Give a bounding box for every leukocyte visible.
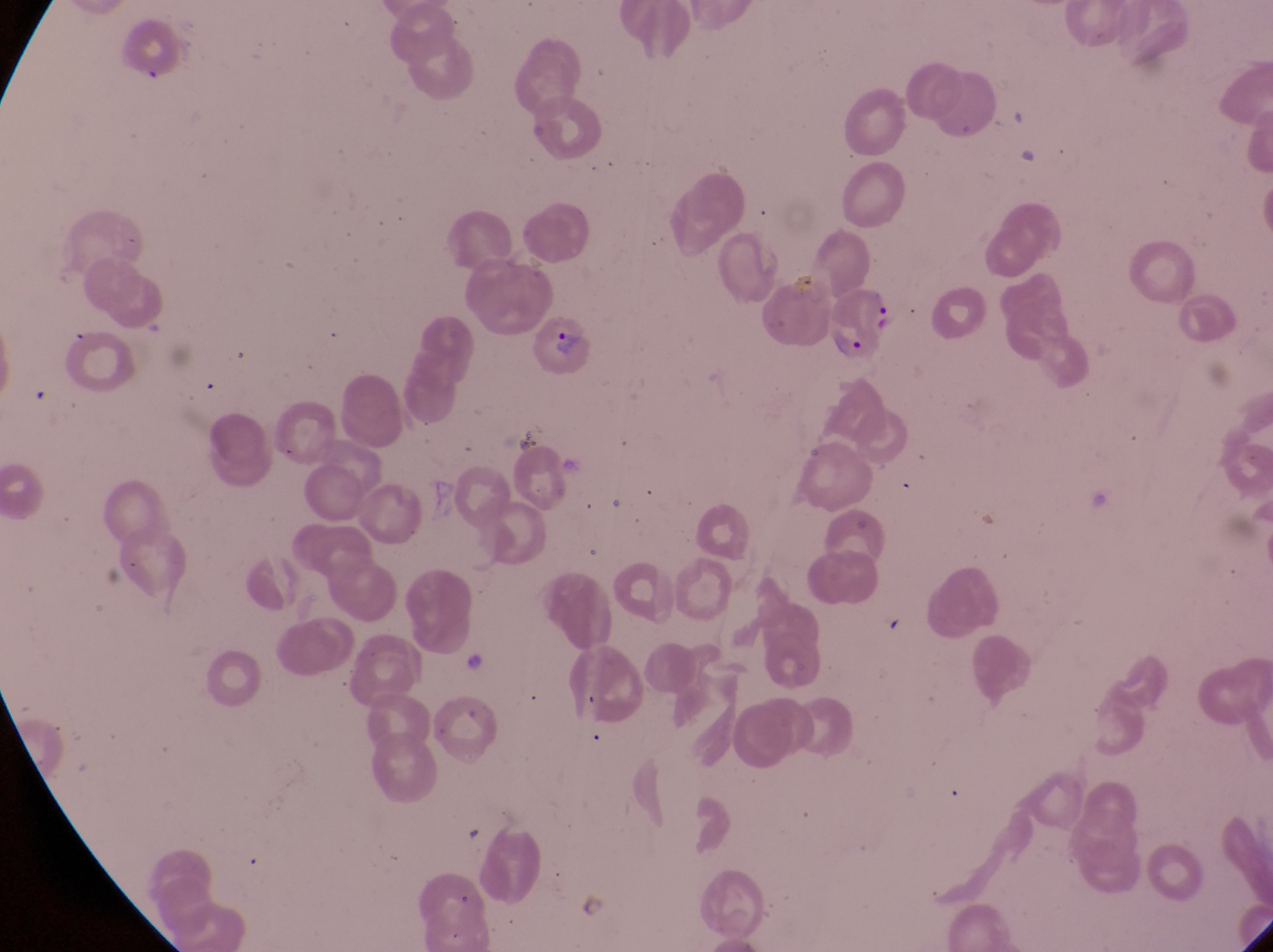
No leukocytes observed.

Approximate bounding boxes as [left, top, right, bottom] in pixels. Parasitised red blood cell locations: [821, 277, 903, 365], [527, 313, 596, 376]. Sample from Uganda. Thin blood smear. Magnification of 1000x. Image is 1273×952 pixels. One field of view. Captured by a smartphone held over the eyepiece of an Olympus CX-23 microscope.